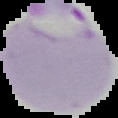 Image is 118×118 pixels. Segmented cell region on a black background. From a thin blood film. Malaria status: parasitized.